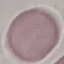

Result: no malaria parasites seen. Cell patch, automatically extracted from a larger field of view and resized to 64 × 64 pixels. Giemsa-stained preparation. Acquired by smartphone through the microscope eyepiece. Thin blood smear.